Report the malaria status of this cell.
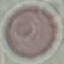

It is uninfected.

capture = smartphone through the microscope eyepiece
preparation = thin blood smear
image type = cell patch, automatically extracted from a larger field of view and resized to 64 × 64 pixels
stain = Giemsa